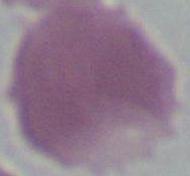
Summary:
  - Identification: red blood cell
  - Modality: micrograph
  - Magnification: 1000x